Classify this cell by malaria status.
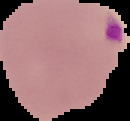

Parasitized.

The area outside the segmented cell region is set to black. Image is 130×121 pixels. From a thin blood smear.